Report the malaria status of this cell.
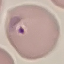

It is parasitized.

Giemsa-stained preparation. Thin blood smear. Automatically extracted cell patch, resized to 64 × 64 pixels. Photographed with a smartphone camera at the microscope eyepiece.